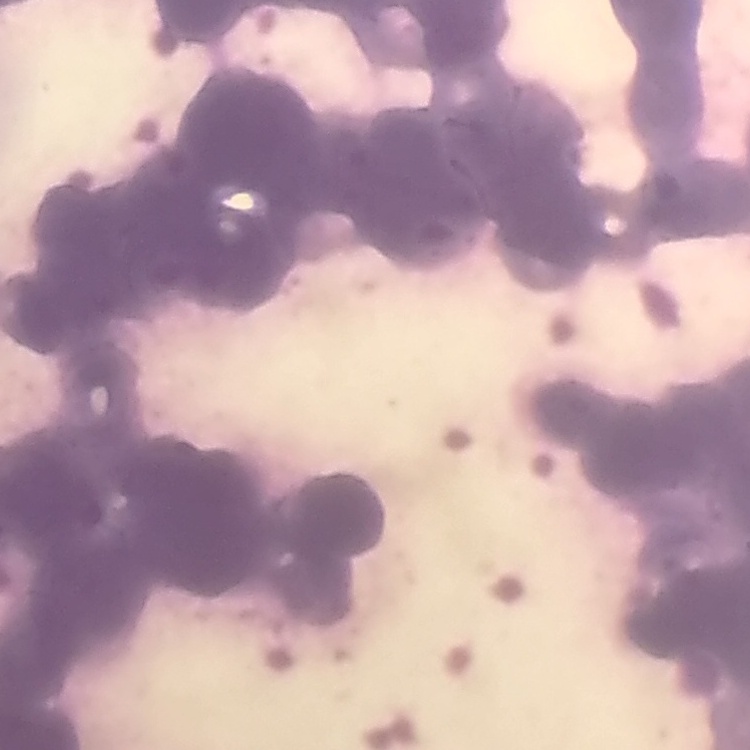 The red blood cells exhibit rouleaux formation. Thin peripheral smear. Square crop of a larger photomicrograph. Stained with either Field's or Giemsa.